Assess for parasitized red blood cells.
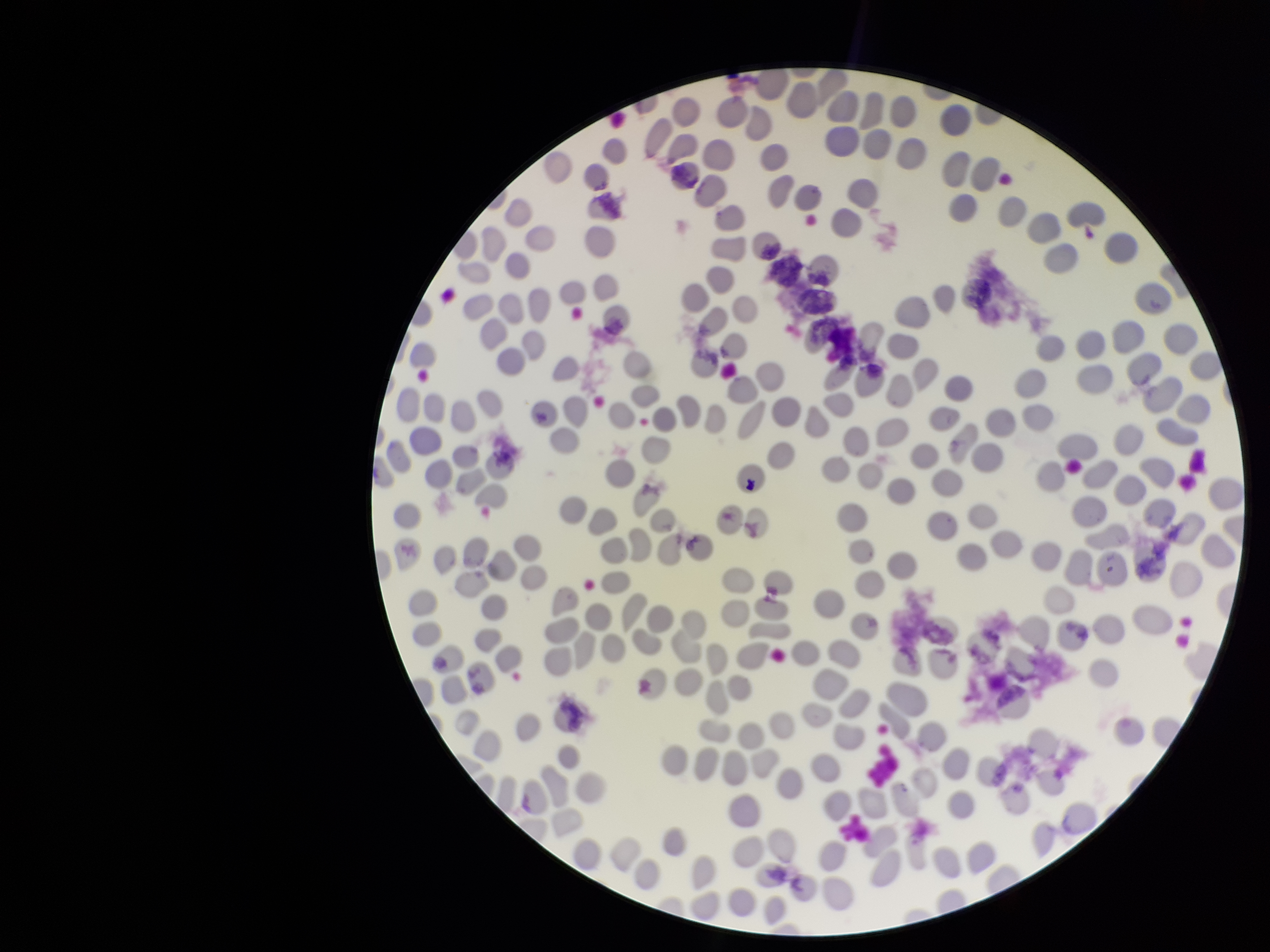

None identified.

One field from this slide. Red blood cell count: 248. Parasitized red blood cell count: 0. Patient malaria status: negative. Stained with Giemsa. Photographed through the microscope eyepiece with a smartphone camera. Preparation: thin. Image is 1270×952 pixels.